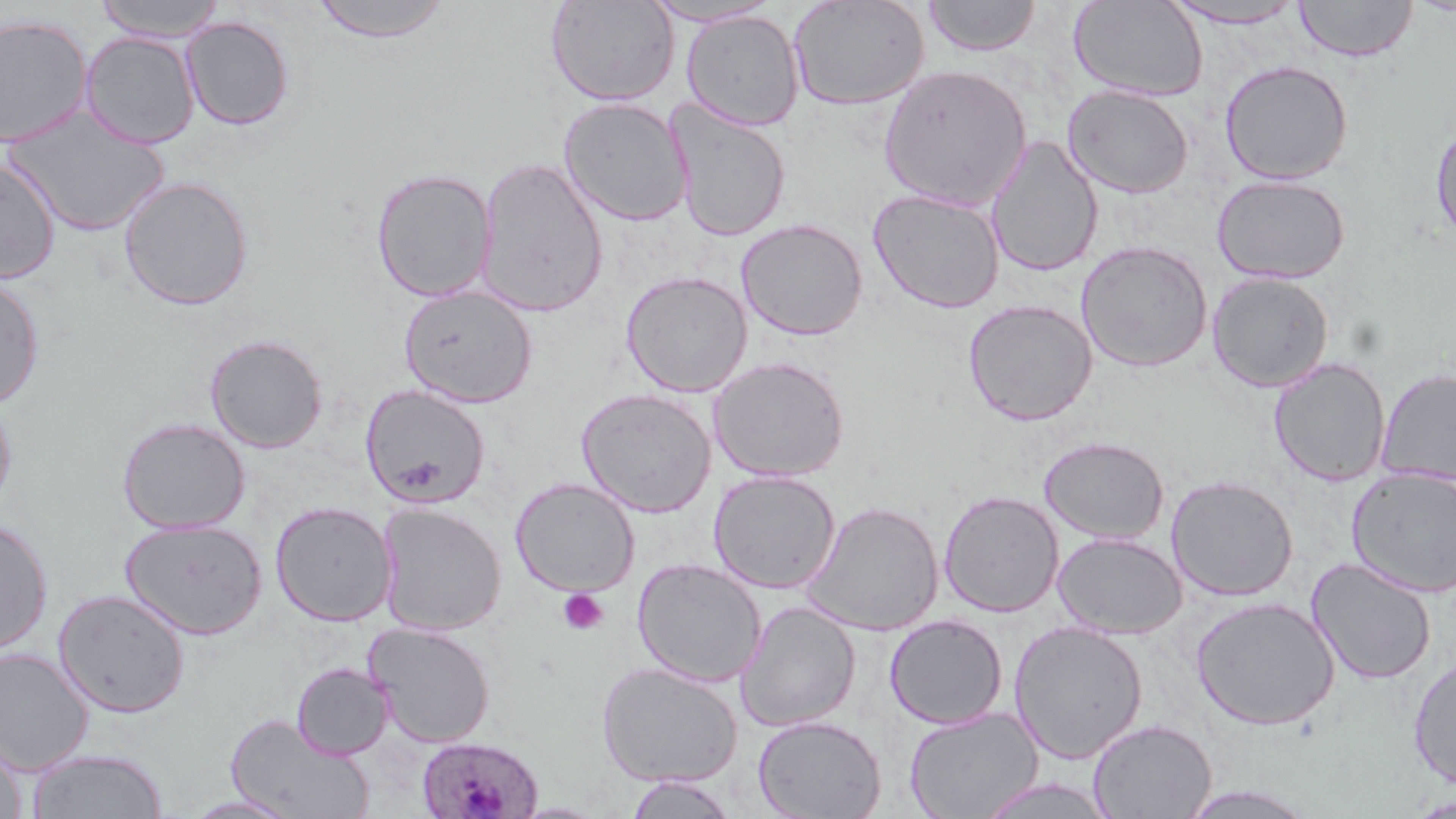
Summary:
  - Coordinate format: approximate bounding boxes as named x1/y1/x2/y2 corners in pixels
  - Platelet locations: (x1=558, y1=589, x2=609, y2=635)
  - Plasmodium ovale-infected red blood cell locations: (x1=415, y1=735, x2=544, y2=819)
  - Uninfected red blood cell locations: (x1=93, y1=0, x2=228, y2=42), (x1=310, y1=0, x2=455, y2=44), (x1=545, y1=0, x2=680, y2=107), (x1=640, y1=0, x2=784, y2=27), (x1=788, y1=0, x2=931, y2=111), (x1=922, y1=0, x2=1042, y2=57), (x1=1069, y1=0, x2=1209, y2=101), (x1=1294, y1=0, x2=1418, y2=62), (x1=1162, y1=1, x2=1309, y2=29), (x1=681, y1=10, x2=804, y2=131), (x1=0, y1=14, x2=93, y2=148), (x1=180, y1=16, x2=294, y2=130), (x1=80, y1=32, x2=199, y2=148), (x1=1219, y1=60, x2=1354, y2=185), (x1=878, y1=64, x2=1032, y2=211), (x1=1063, y1=84, x2=1194, y2=198), (x1=558, y1=97, x2=693, y2=227), (x1=666, y1=100, x2=791, y2=243), (x1=3, y1=107, x2=170, y2=238), (x1=1431, y1=119, x2=1456, y2=244), (x1=985, y1=135, x2=1104, y2=278), (x1=475, y1=156, x2=610, y2=318), (x1=0, y1=157, x2=61, y2=284), (x1=371, y1=167, x2=497, y2=302), (x1=1212, y1=174, x2=1351, y2=285), (x1=118, y1=176, x2=254, y2=310), (x1=868, y1=188, x2=1005, y2=314), (x1=735, y1=218, x2=868, y2=341), (x1=1076, y1=241, x2=1213, y2=372), (x1=620, y1=270, x2=753, y2=398), (x1=1207, y1=272, x2=1334, y2=393), (x1=0, y1=274, x2=44, y2=409), (x1=398, y1=284, x2=538, y2=408), (x1=963, y1=299, x2=1098, y2=426), (x1=205, y1=334, x2=328, y2=453), (x1=709, y1=356, x2=850, y2=482), (x1=1268, y1=357, x2=1391, y2=487), (x1=1375, y1=367, x2=1456, y2=487), (x1=360, y1=383, x2=491, y2=509), (x1=576, y1=387, x2=717, y2=517), (x1=0, y1=393, x2=17, y2=514), (x1=117, y1=417, x2=251, y2=535), (x1=1039, y1=436, x2=1170, y2=544), (x1=1347, y1=468, x2=1456, y2=598), (x1=708, y1=470, x2=840, y2=594), (x1=1166, y1=475, x2=1299, y2=601), (x1=511, y1=478, x2=640, y2=597), (x1=939, y1=490, x2=1064, y2=617), (x1=802, y1=500, x2=943, y2=636), (x1=270, y1=501, x2=398, y2=626), (x1=376, y1=503, x2=507, y2=636), (x1=0, y1=518, x2=53, y2=655), (x1=119, y1=518, x2=267, y2=639), (x1=1053, y1=532, x2=1188, y2=639), (x1=1306, y1=557, x2=1437, y2=685), (x1=632, y1=558, x2=766, y2=687), (x1=53, y1=588, x2=190, y2=718), (x1=1190, y1=596, x2=1341, y2=730), (x1=735, y1=600, x2=860, y2=732), (x1=884, y1=614, x2=1008, y2=729), (x1=1009, y1=621, x2=1148, y2=763), (x1=363, y1=622, x2=496, y2=748), (x1=0, y1=647, x2=95, y2=774), (x1=1408, y1=654, x2=1456, y2=789), (x1=596, y1=661, x2=743, y2=788), (x1=291, y1=663, x2=393, y2=759), (x1=904, y1=706, x2=1043, y2=819), (x1=226, y1=712, x2=373, y2=819), (x1=752, y1=715, x2=886, y2=819), (x1=1088, y1=719, x2=1216, y2=818), (x1=0, y1=734, x2=27, y2=819), (x1=26, y1=747, x2=168, y2=818), (x1=623, y1=774, x2=741, y2=818), (x1=974, y1=777, x2=1119, y2=819), (x1=1178, y1=785, x2=1319, y2=818), (x1=181, y1=794, x2=303, y2=817), (x1=1409, y1=794, x2=1456, y2=818)
  - Slide-level diagnosis: Plasmodium ovale
  - Preparation: thin blood smear
  - Modality: light microscopy
  - Image size: 1456×819 pixels
  - Magnification: 1000x
  - Stain: May-Grünwald-Giemsa
  - Field of view: one of a larger specimen